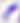
{
  "magnification": "400x",
  "modality": "photomicrograph",
  "identification": "Toxoplasma gondii"
}